Report the malaria status of this cell.
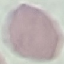
It is uninfected.

{
  "stain": "Giemsa",
  "preparation": "thin blood film",
  "image_type": "cell patch, automatically extracted from a larger field of view and resized to 64 × 64 pixels",
  "capture": "smartphone camera at the microscope eyepiece"
}